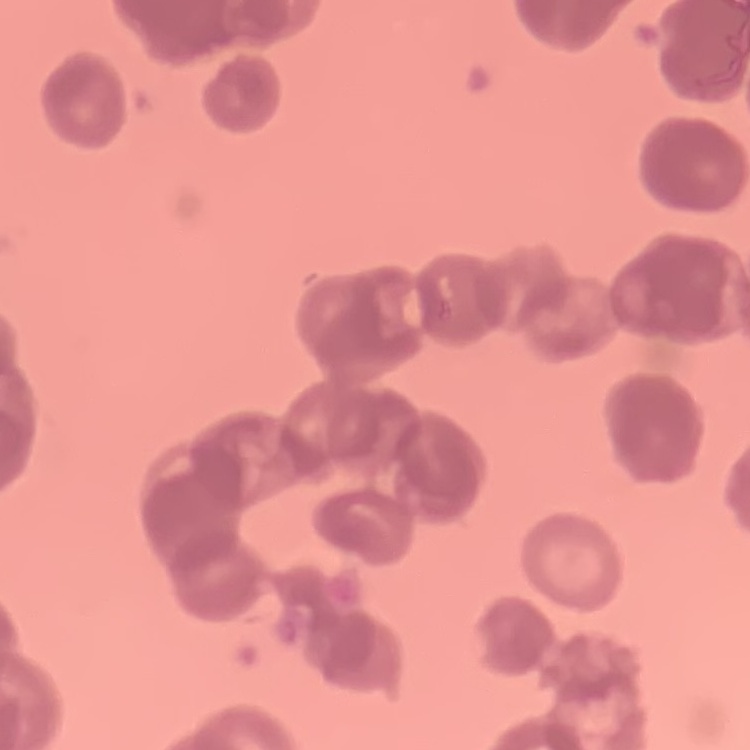
erythrocyte morphology = rouleaux formation
image type = one tile cut from a larger photomicrograph
preparation = thin peripheral smear
stain = Field's or Giemsa